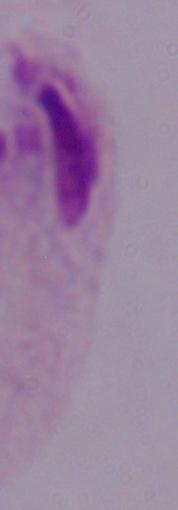
Summary:
  - Modality: photomicrograph
  - Identification: trichomonad
  - Magnification: 1000x